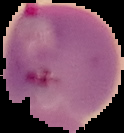
Summary:
  - Malaria status: parasitized
  - Image type: cell region segmented out of the field of view; surrounding area masked to black
  - Preparation: thin blood smear
  - Image size: 124×133 pixels